Report the malaria status of this cell.
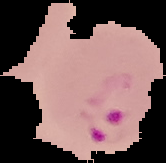

It is parasitized.

Image is 166×163 pixels. From a thin blood smear. The area outside the segmented cell region is set to black.